Report the malaria status of this cell.
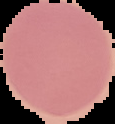

Uninfected.

Image is 115×124 pixels. Cell region segmented out of the field of view; the surrounding area is masked to black. From a thin blood film.